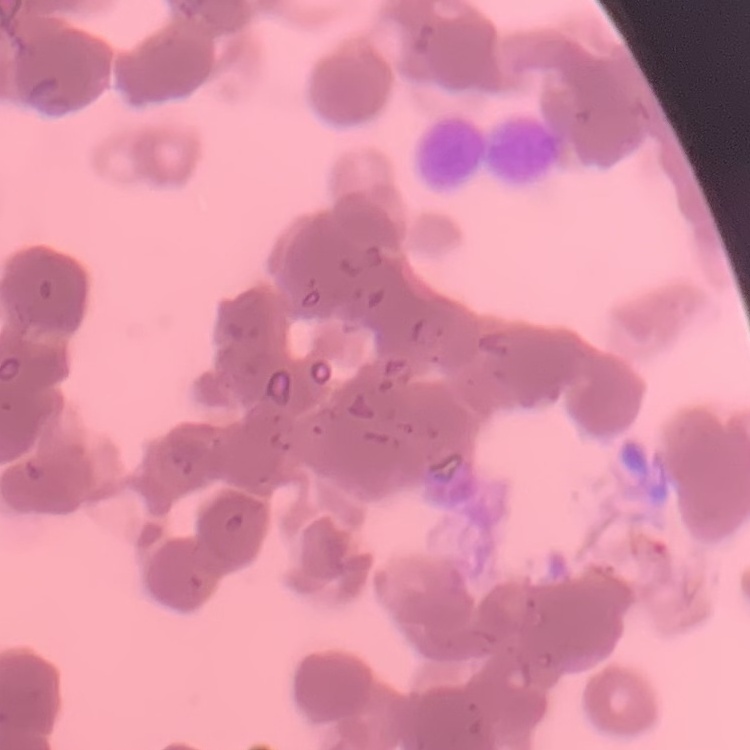

erythrocyte morphology = rouleaux formation
preparation = thin blood film
stain = Field's or Giemsa
image type = one tile cut from a larger photomicrograph